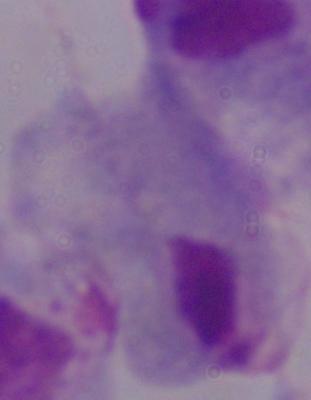

magnification = 1000x
identification = trichomonad
modality = micrograph